Classify this cell by malaria status.
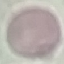

It is uninfected.

Giemsa stain. Thin blood film. Photographed with a smartphone camera at the microscope eyepiece. Automatically extracted cell patch, resized to 64 × 64 pixels.